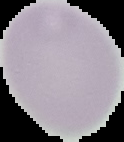 Image is 124×142 pixels. From a thin blood smear. Cell region segmented out of the field of view; the surrounding area is masked to black. Result: no malaria parasites detected.